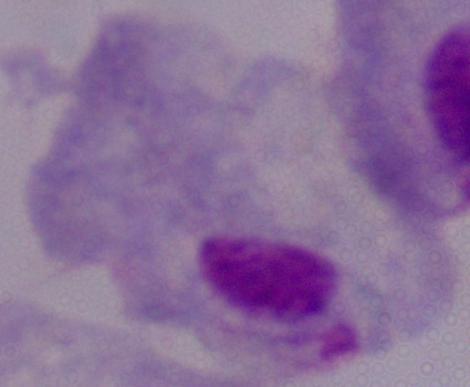

A trichomonad is seen. Photomicrograph. Captured at 1000x magnification.